Identify the cell.
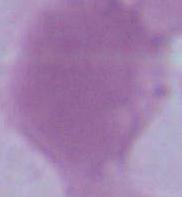
This is an erythrocyte.

Summary:
  - Modality: photomicrograph
  - Magnification: 1000x